Report the malaria status of this cell.
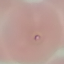
It is parasitized.

Giemsa stain. Automatically extracted cell patch, resized to 64 × 64 pixels. Acquired by smartphone through the microscope eyepiece. Thin blood smear.